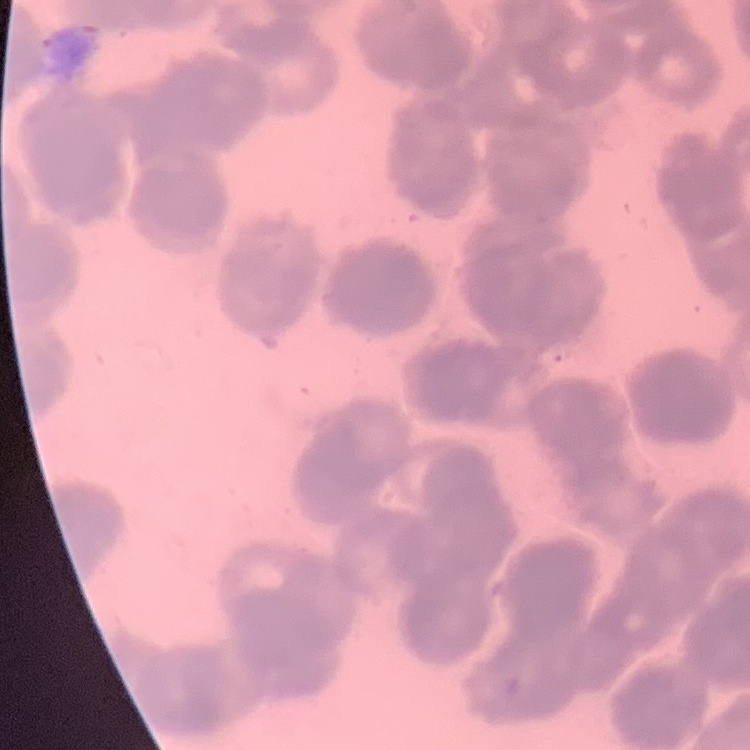 The erythrocytes exhibit rouleaux formation. One tile cut from a larger photomicrograph. Stained with either Field's or Giemsa. Thin blood film.